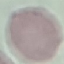
malaria status = uninfected
image type = automatically extracted cell patch, resized to 64 × 64 pixels
preparation = thin blood film
stain = Giemsa
capture = smartphone camera at the microscope eyepiece